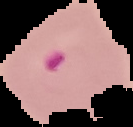 From a thin blood smear. The area outside the segmented cell region is set to black. Malaria status: parasitized. Image is 133×127 pixels.